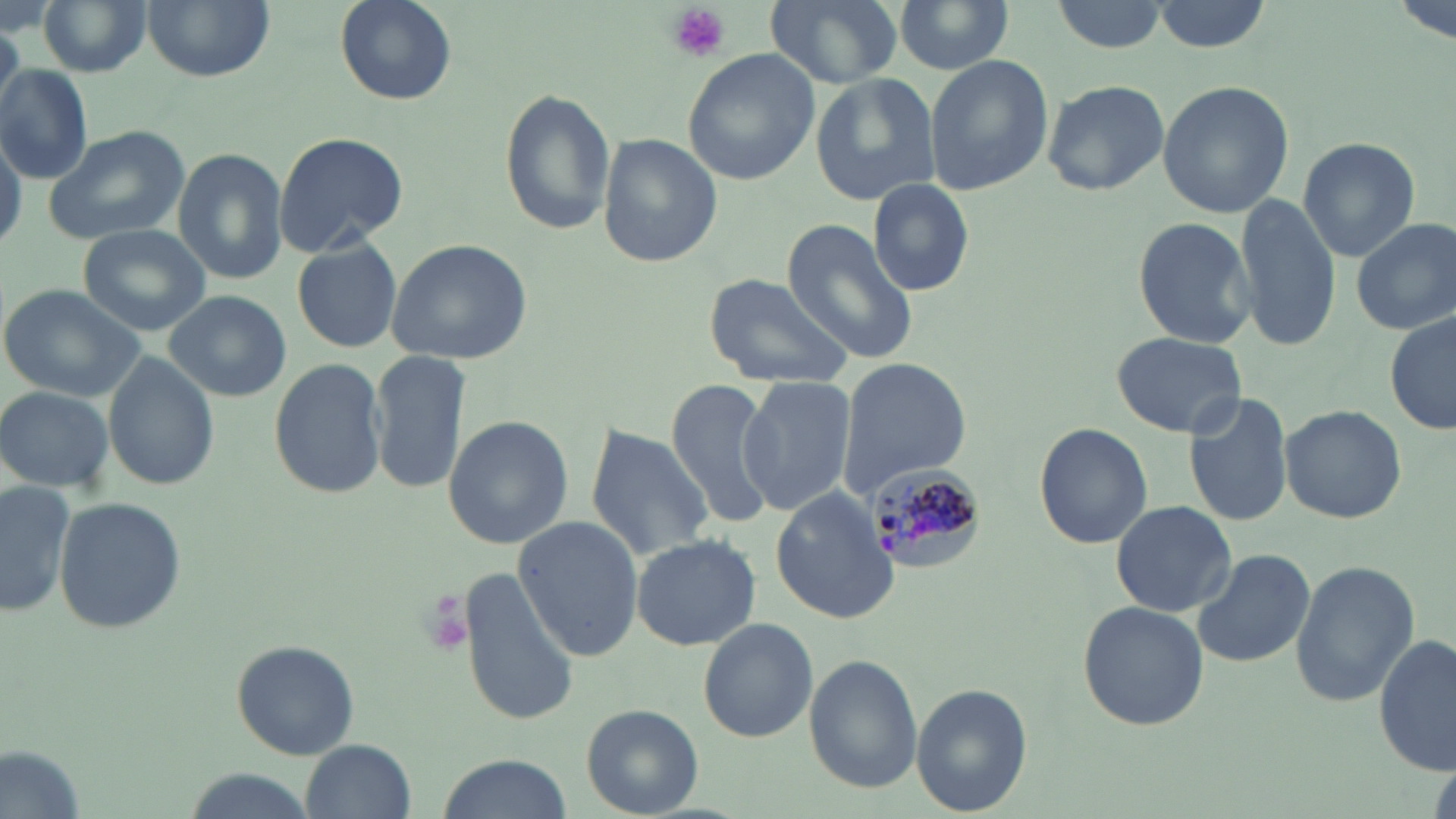 Approximate bounding boxes as (x1,y1)-(x2,y2) corner pairs in pixels. Plasmodium malariae-infected red blood cell locations: (858,466)-(988,579). Uninfected red blood cell locations: (141,0)-(276,81), (336,0)-(457,104), (765,0)-(903,91), (894,0)-(1016,76), (1152,0)-(1274,51), (36,1)-(152,77), (1049,1)-(1171,53), (683,51)-(818,185), (925,56)-(1054,194), (0,66)-(94,184), (809,72)-(943,206), (1041,78)-(1169,197), (1158,80)-(1298,218), (498,91)-(616,237), (41,124)-(192,248), (271,130)-(407,256), (0,133)-(25,255), (599,133)-(721,267), (1297,136)-(1421,260), (172,147)-(289,287), (867,179)-(974,294), (820,187)-(949,327), (1236,195)-(1341,348), (1134,214)-(1259,347), (1352,216)-(1456,336), (780,220)-(920,368), (76,223)-(211,336), (386,239)-(531,365), (294,241)-(402,352), (702,270)-(854,391), (0,283)-(147,402), (163,290)-(291,402), (1386,312)-(1455,437), (1111,331)-(1247,437), (370,350)-(470,492), (102,355)-(219,490), (268,355)-(389,500), (836,357)-(972,496), (736,377)-(853,514), (665,378)-(778,528), (0,385)-(116,491), (1185,391)-(1294,527), (1280,403)-(1405,523), (441,414)-(573,548), (1033,422)-(1152,548), (585,425)-(715,561), (0,480)-(77,616), (773,487)-(899,623), (52,495)-(186,635), (1110,500)-(1238,617), (513,515)-(644,659), (631,534)-(761,650), (1192,546)-(1315,669), (1289,559)-(1420,705), (456,564)-(583,727), (1077,601)-(1209,730), (698,617)-(817,742), (1376,634)-(1456,774), (229,640)-(360,759), (805,655)-(920,792), (912,684)-(1029,815), (582,705)-(701,815), (302,740)-(417,819), (1,743)-(89,819), (438,753)-(569,819), (179,770)-(320,819). Platelet locations: (666,3)-(730,62), (422,595)-(472,652). Slide-level diagnosis: Plasmodium malariae. Optical microscopy. May-Grünwald-Giemsa stain. Thin blood smear. Single field of view. Image is 1456×819 pixels. 1000x magnification.